Comment on the morphology of the red blood cells.
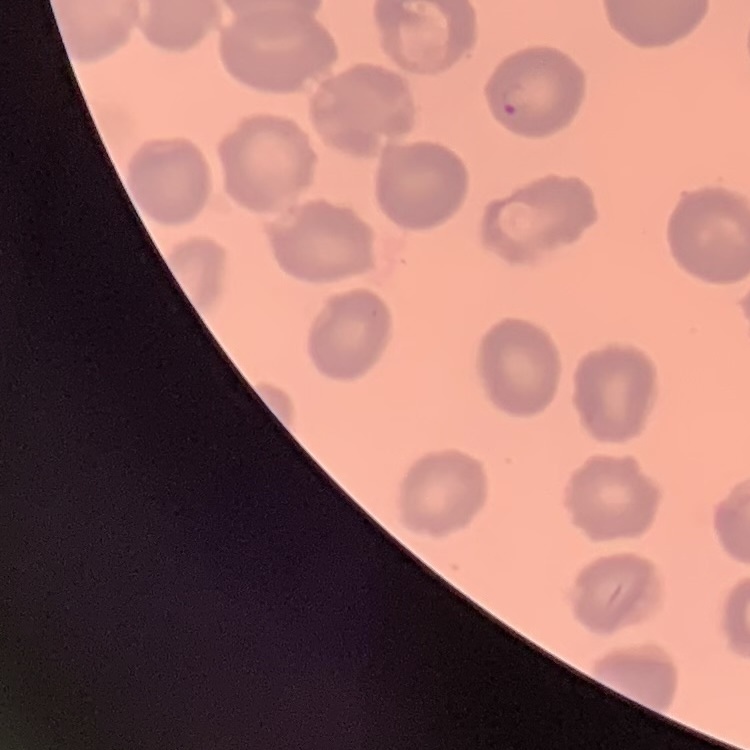
No rouleaux formation.

Stained with either Field's or Giemsa. Thin peripheral smear. One tile cut from a larger photomicrograph.